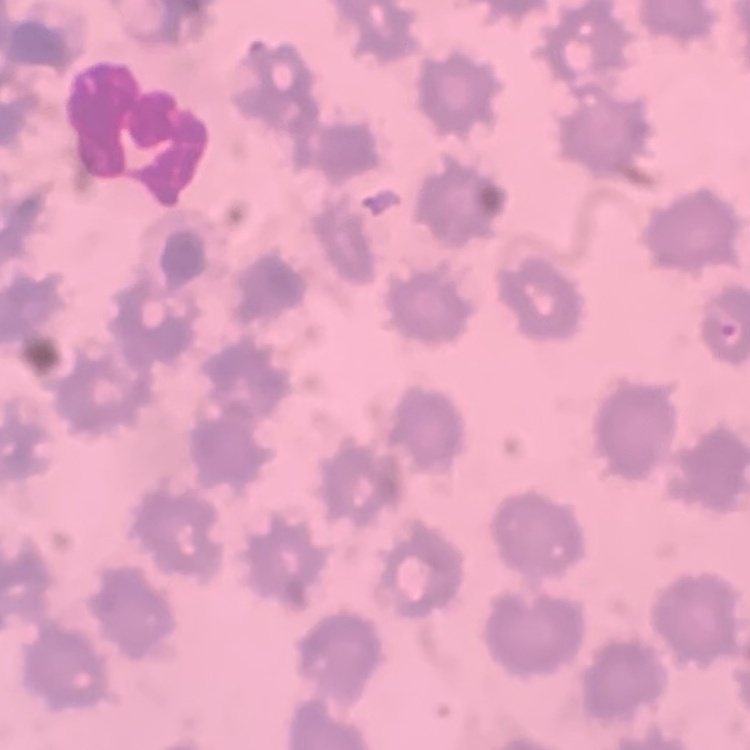 The red blood cells exhibit no rouleaux formation. Stained with either Field's or Giemsa. Thin blood film. Square crop of a larger photomicrograph.